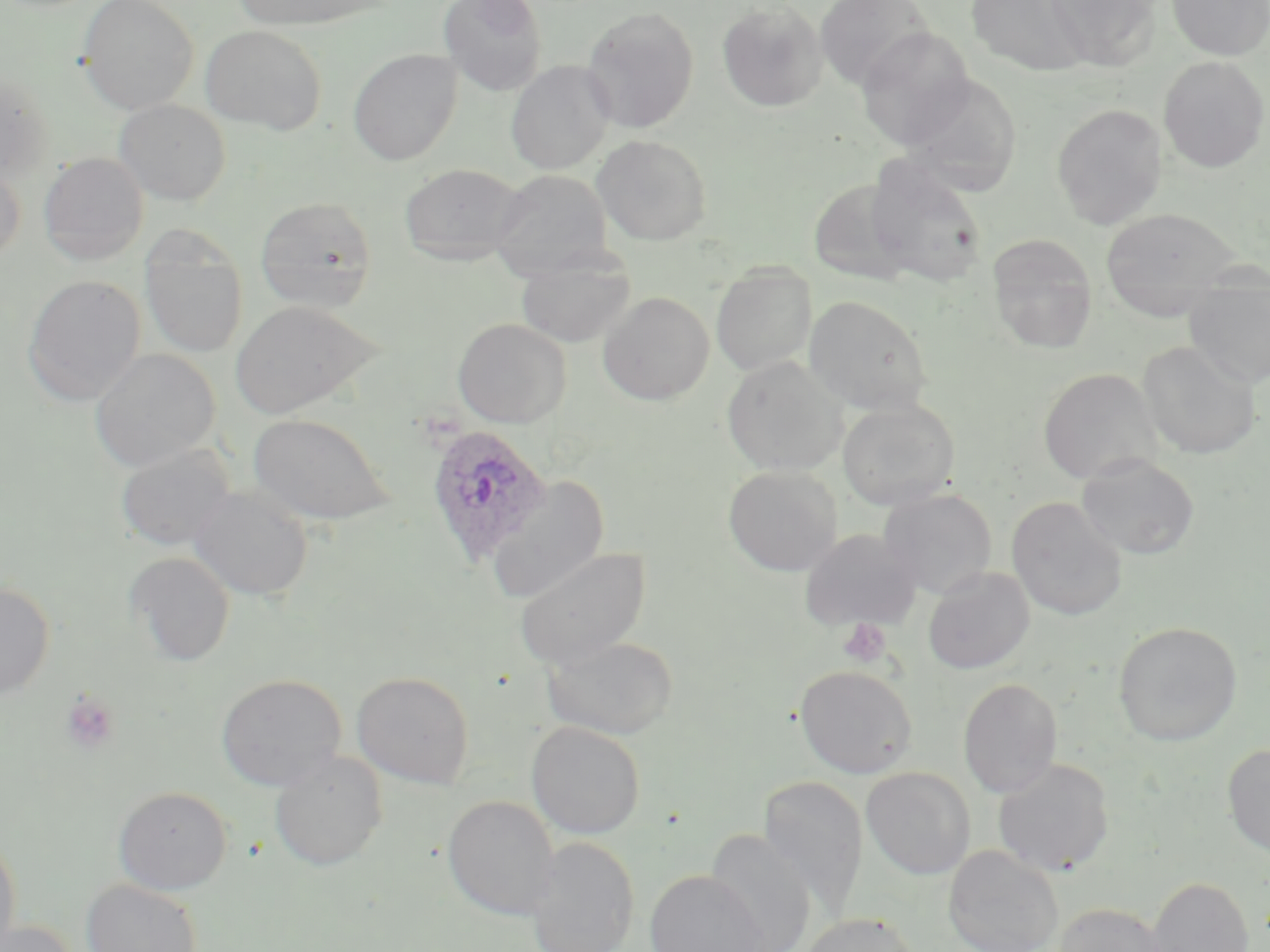

Plasmodium ovale-infected red blood cell locations = approximate bounding boxes as [x1, y1, x2, y2] in pixels: [424, 423, 552, 565]
slide-level diagnosis = Plasmodium ovale
modality = optical microscopy
image size = 1270×952 pixels
field of view = single
stain = May-Grünwald-Giemsa
preparation = thin blood smear
magnification = 1000x
platelet locations = approximate bounding boxes as [x1, y1, x2, y2] in pixels: [838, 617, 893, 668], [60, 690, 121, 754]
uninfected red blood cell locations = approximate bounding boxes as [x1, y1, x2, y2] in pixels: [78, 0, 199, 114], [233, 0, 382, 30], [439, 0, 547, 95], [815, 0, 934, 90], [968, 0, 1087, 75], [1043, 0, 1161, 70], [1166, 0, 1270, 60], [716, 1, 828, 112], [580, 6, 700, 134], [201, 25, 326, 134], [855, 27, 976, 149], [348, 49, 462, 165], [1158, 56, 1269, 172], [505, 60, 615, 174], [0, 71, 53, 179], [899, 74, 1022, 194], [114, 99, 231, 205], [1051, 103, 1168, 229], [593, 135, 712, 245], [38, 152, 149, 265], [865, 159, 988, 286], [0, 162, 26, 265], [398, 163, 529, 264], [490, 168, 613, 278], [255, 196, 378, 313], [1100, 207, 1241, 314], [140, 230, 248, 360], [987, 236, 1098, 354], [515, 252, 636, 349], [711, 265, 816, 377], [22, 274, 146, 406], [1185, 285, 1270, 387], [597, 291, 715, 405], [803, 295, 932, 414], [229, 300, 380, 419], [452, 317, 571, 428], [1137, 340, 1261, 459], [90, 349, 220, 471], [721, 356, 848, 476], [1037, 367, 1163, 485], [837, 400, 960, 510], [247, 412, 393, 526], [114, 443, 235, 551], [1076, 453, 1200, 560], [722, 465, 843, 576], [487, 475, 610, 602], [189, 485, 313, 601], [879, 488, 998, 599], [1006, 496, 1127, 621], [799, 529, 921, 632], [513, 546, 652, 669], [125, 551, 236, 667], [923, 566, 1035, 674], [0, 581, 55, 699], [1112, 621, 1242, 746], [540, 633, 679, 740], [795, 664, 917, 778], [351, 671, 475, 789], [216, 673, 347, 791], [958, 677, 1063, 798], [526, 721, 646, 839], [1222, 744, 1270, 858], [269, 751, 387, 871], [992, 758, 1115, 877], [861, 767, 975, 880], [758, 774, 869, 917], [112, 786, 232, 894], [443, 794, 559, 921], [704, 828, 817, 952], [0, 831, 21, 952], [525, 837, 640, 952], [943, 844, 1064, 952], [644, 869, 771, 952], [1146, 875, 1254, 952], [81, 878, 202, 952], [1053, 902, 1173, 952], [800, 912, 920, 952], [1, 920, 81, 952]